Give the position of every malaria parasite, noting whether each is a trophozoite, schizont, or gametocyte.
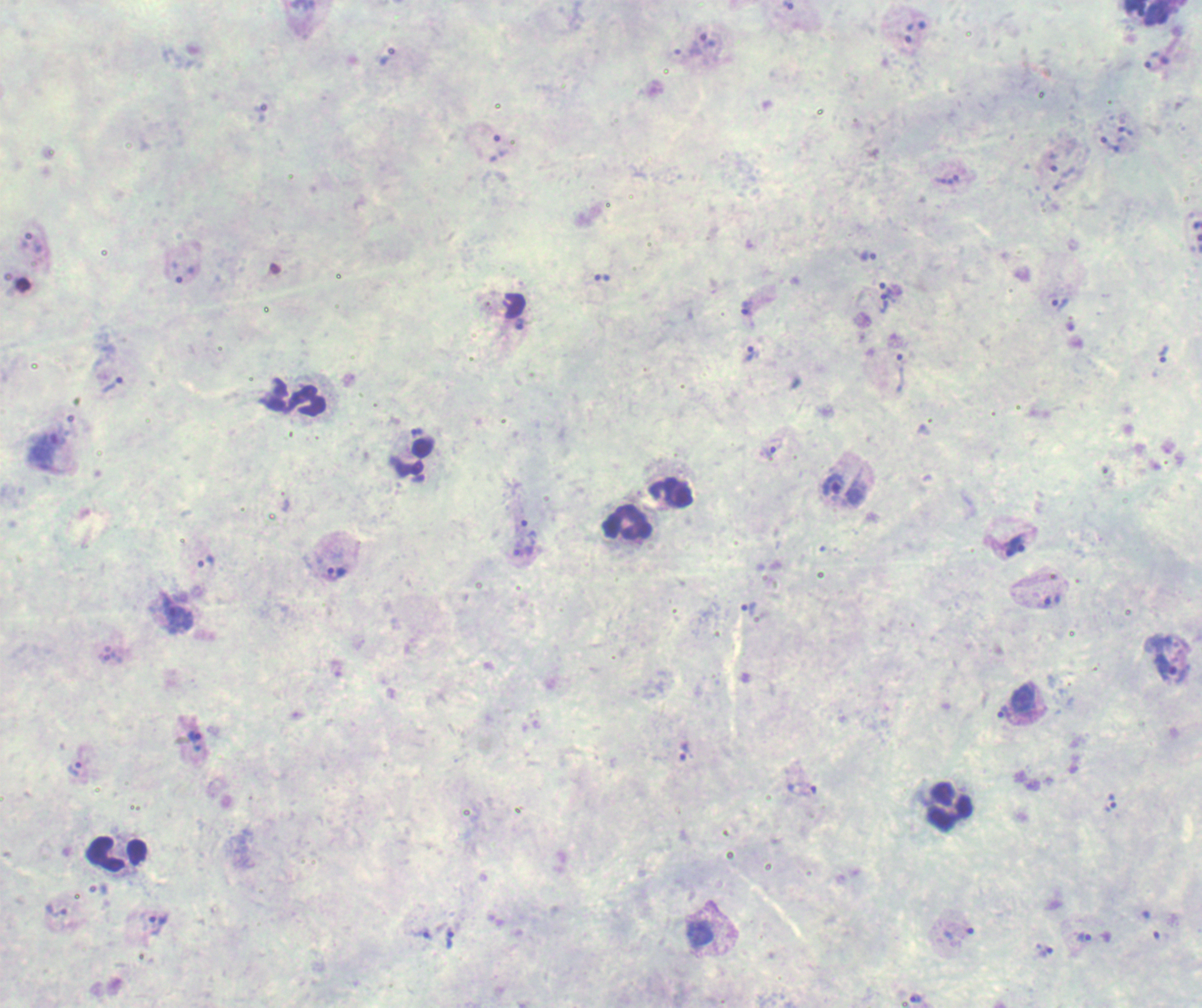

Approximate object centers, in pixels from the top-left corner.
Trophozoites: (x=786, y=5), (x=909, y=32), (x=709, y=41), (x=387, y=56), (x=1156, y=60), (x=260, y=113), (x=1125, y=131), (x=1110, y=145), (x=940, y=180), (x=953, y=180), (x=868, y=256), (x=602, y=278), (x=891, y=289), (x=1060, y=302), (x=884, y=303), (x=746, y=308), (x=522, y=324), (x=749, y=353), (x=1163, y=355), (x=906, y=357), (x=112, y=384), (x=43, y=449), (x=767, y=450), (x=530, y=530), (x=1014, y=546), (x=522, y=552), (x=206, y=563), (x=337, y=572), (x=1051, y=601), (x=749, y=607), (x=177, y=613), (x=110, y=657), (x=1171, y=668), (x=1003, y=711), (x=195, y=738), (x=683, y=752), (x=76, y=769), (x=801, y=789), (x=1111, y=802), (x=57, y=911), (x=159, y=925), (x=700, y=934), (x=958, y=934), (x=421, y=935), (x=1084, y=938), (x=450, y=939), (x=1046, y=951), (x=916, y=997).
Gametocytes: (x=834, y=485), (x=1023, y=697).
No schizont forms observed.

Approximate object centers, in pixels from the top-left corner. Leukocyte locations: (x=1147, y=12), (x=292, y=397), (x=411, y=458), (x=671, y=493), (x=626, y=524), (x=949, y=807), (x=117, y=854). Background quality: poor. Image is 1202×1008 pixels. Previously used in a real diagnosis. Captured at 100x magnification. Single field of view. Thick blood smear. Romanowsky-stained preparation.